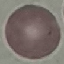

malaria status = uninfected
capture = smartphone camera at the microscope eyepiece
image type = automatically extracted cell patch, resized to 64 × 64 pixels
stain = Giemsa
preparation = thin smear